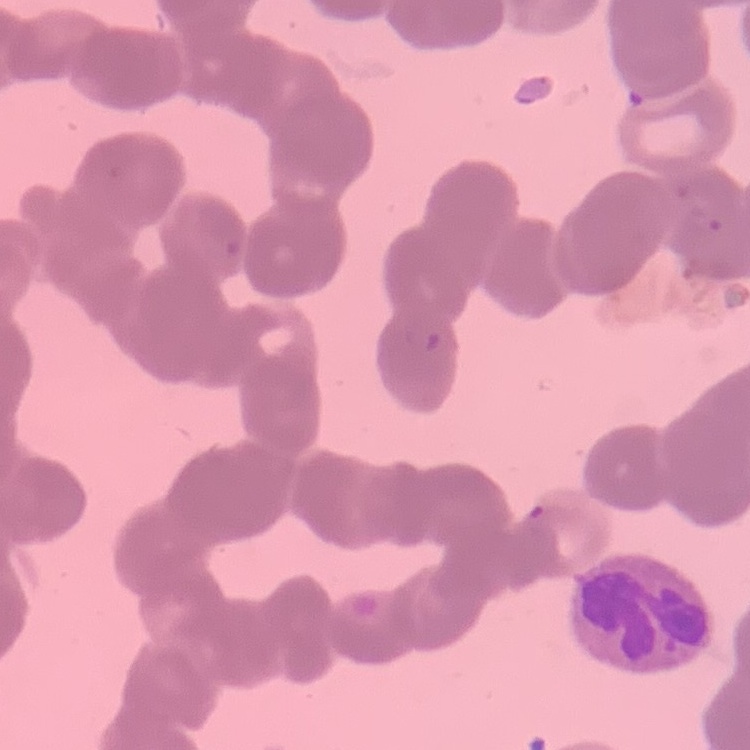 The red blood cells exhibit rouleaux formation. Field's or Giemsa stain. One tile cut from a larger photomicrograph. Thin peripheral smear.